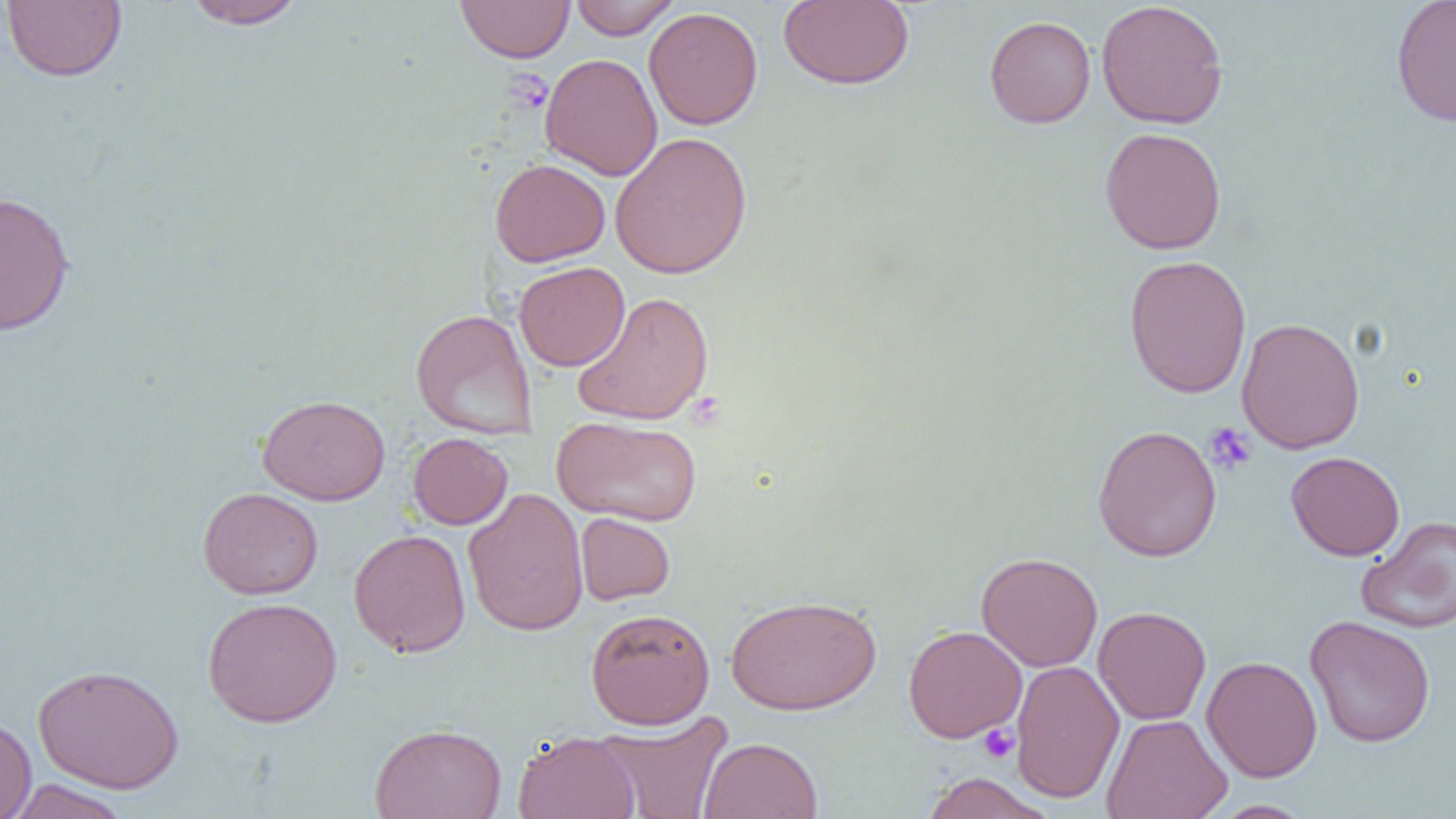

{
  "slide_level_diagnosis": "negative for blood parasites",
  "modality": "light microscopy",
  "field_of_view": "single",
  "uninfected_red_blood_cell_locations": "approximate bounding boxes as (x1,y1)-(x2,y2) corner pairs in pixels: (183,0)-(307,30), (455,0)-(576,63), (569,0)-(681,39), (778,0)-(914,90), (1390,0)-(1456,127), (2,1)-(127,82), (1096,1)-(1229,129), (643,7)-(763,130), (984,15)-(1096,128), (540,53)-(663,181), (1099,126)-(1227,255), (609,131)-(753,279), (490,159)-(610,266), (0,191)-(76,336), (1123,254)-(1252,398), (514,261)-(630,371), (573,291)-(715,425), (410,308)-(537,439), (1236,317)-(1365,454), (257,394)-(390,506), (551,415)-(703,527), (1092,424)-(1222,562), (407,432)-(513,530), (1286,451)-(1405,560), (197,487)-(323,599), (463,487)-(589,637), (575,512)-(675,605), (1356,517)-(1455,634), (348,528)-(471,657), (976,552)-(1103,671), (725,594)-(881,715), (202,596)-(342,727), (1093,606)-(1211,725), (585,607)-(715,729), (1304,614)-(1436,748), (903,624)-(1027,743), (1201,655)-(1323,782), (1010,660)-(1125,804), (32,664)-(184,795), (596,710)-(734,819), (1101,713)-(1233,819), (0,714)-(37,818), (369,723)-(507,819), (513,731)-(640,819), (698,737)-(823,819), (920,772)-(1056,818), (7,779)-(133,819), (1211,800)-(1316,819)",
  "preparation": "thin blood smear",
  "image_size": "1456×819 pixels",
  "platelet_locations": "approximate bounding boxes as (x1,y1)-(x2,y2) corner pairs in pixels: (502,69)-(553,115), (1203,422)-(1256,475), (978,724)-(1020,764)",
  "magnification": "1000x"
}